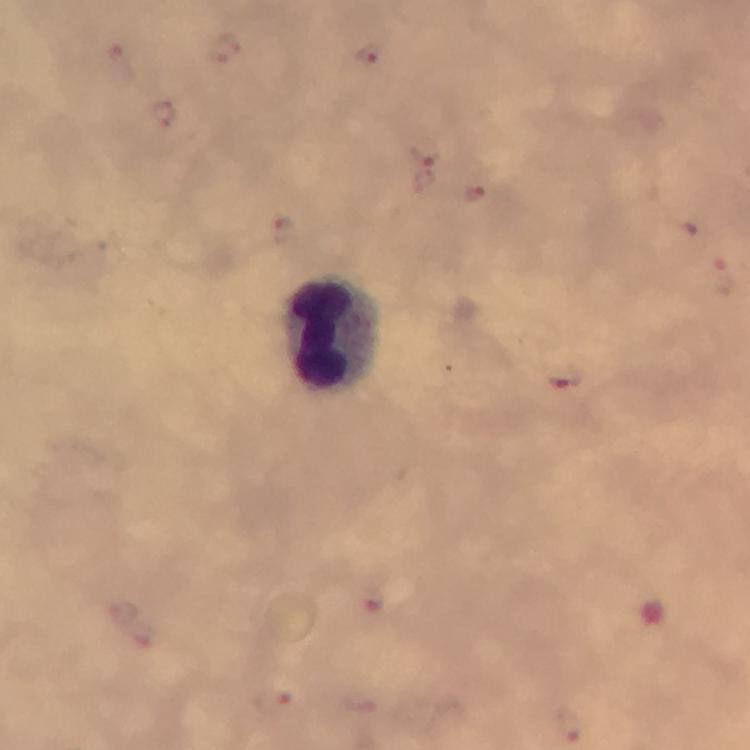

{
  "magnification": "100x",
  "context": "from a malaria diagnostic workup",
  "cropped_from": "one field of view",
  "stain": "Giemsa",
  "capture": "smartphone photograph through a microscope",
  "plasmodium_parasite_locations": "approximate centers as (x, y) in pixels: (368, 53), (162, 113), (425, 152), (473, 193), (280, 229), (721, 277), (562, 377), (372, 604), (272, 700), (568, 727)",
  "image_size": "750×750 pixels",
  "immersion_oil": "applied",
  "preparation": "thick blood film",
  "leukocyte_locations": "approximate centers as (x, y) in pixels: (334, 336)"
}